Point out each leukocyte.
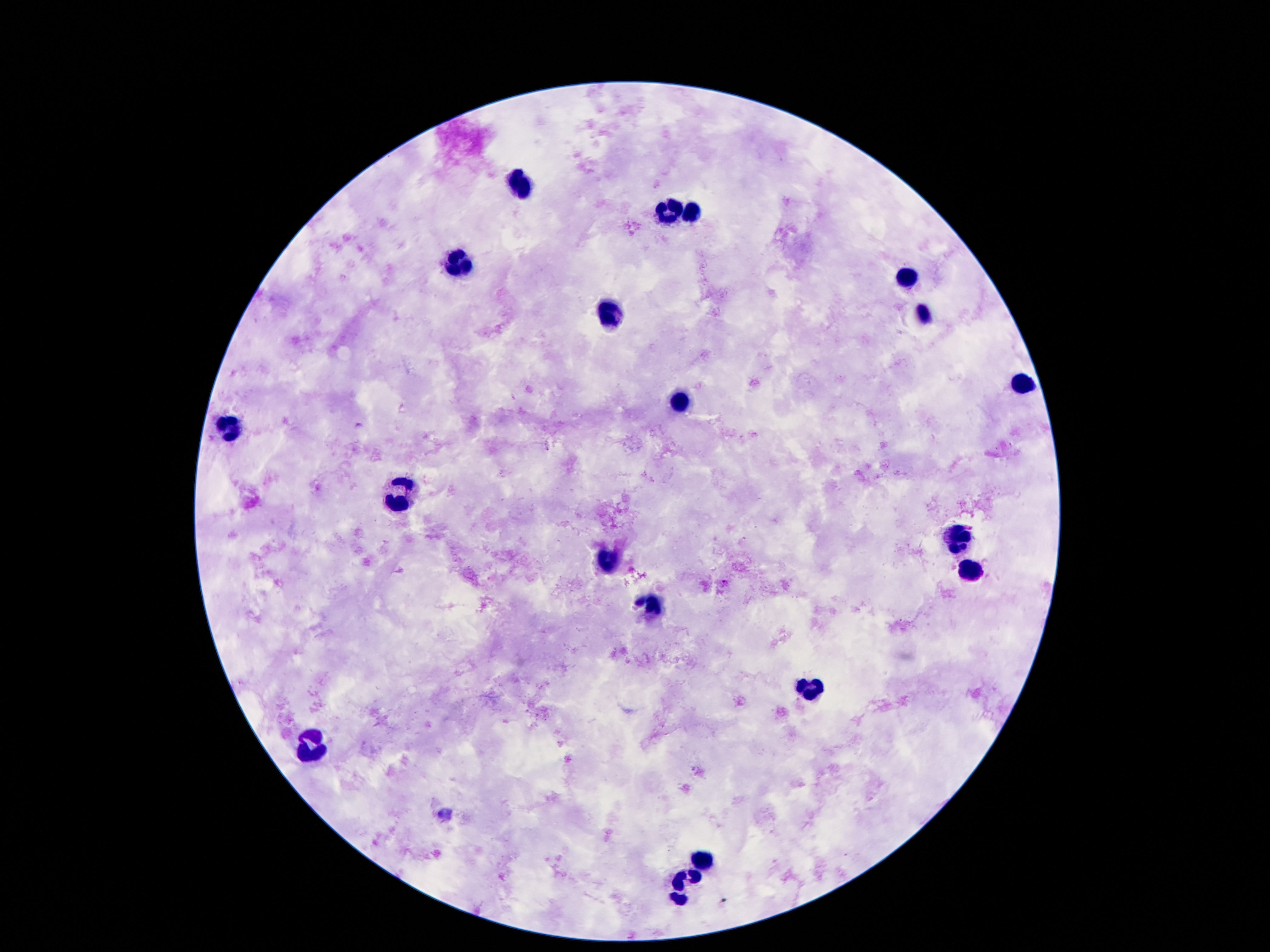

Approximate centers as [x, y] in pixels.
Leukocytes: [517, 184], [666, 210], [693, 211], [458, 260], [906, 279], [609, 311], [920, 315], [1021, 382], [681, 399], [225, 426], [401, 494], [960, 538], [607, 559], [973, 567], [656, 607], [811, 686], [311, 743], [702, 858], [685, 884].

Summary:
  - Patient malaria status: uninfected
  - Capture: smartphone camera through the microscope eyepiece
  - Field of view: one from this slide
  - Stain: Giemsa
  - Image size: 1270×952 pixels
  - Preparation: thick blood film
  - Magnification: 100x